Assess this cell for malaria.
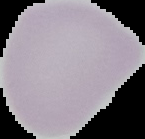

Uninfected.

Segmented cell region on a black background. From a thin blood film. Image is 145×139 pixels.